Name the parasite shown.
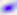

This is Toxoplasma gondii.

Captured at 400x magnification. Micrograph.